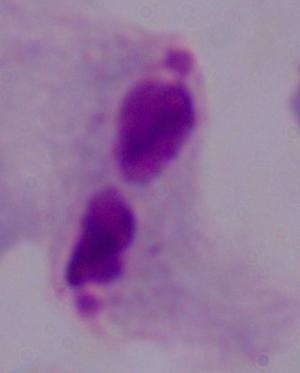

Summary:
  - Magnification: 1000x
  - Identification: trichomonad
  - Modality: photomicrograph